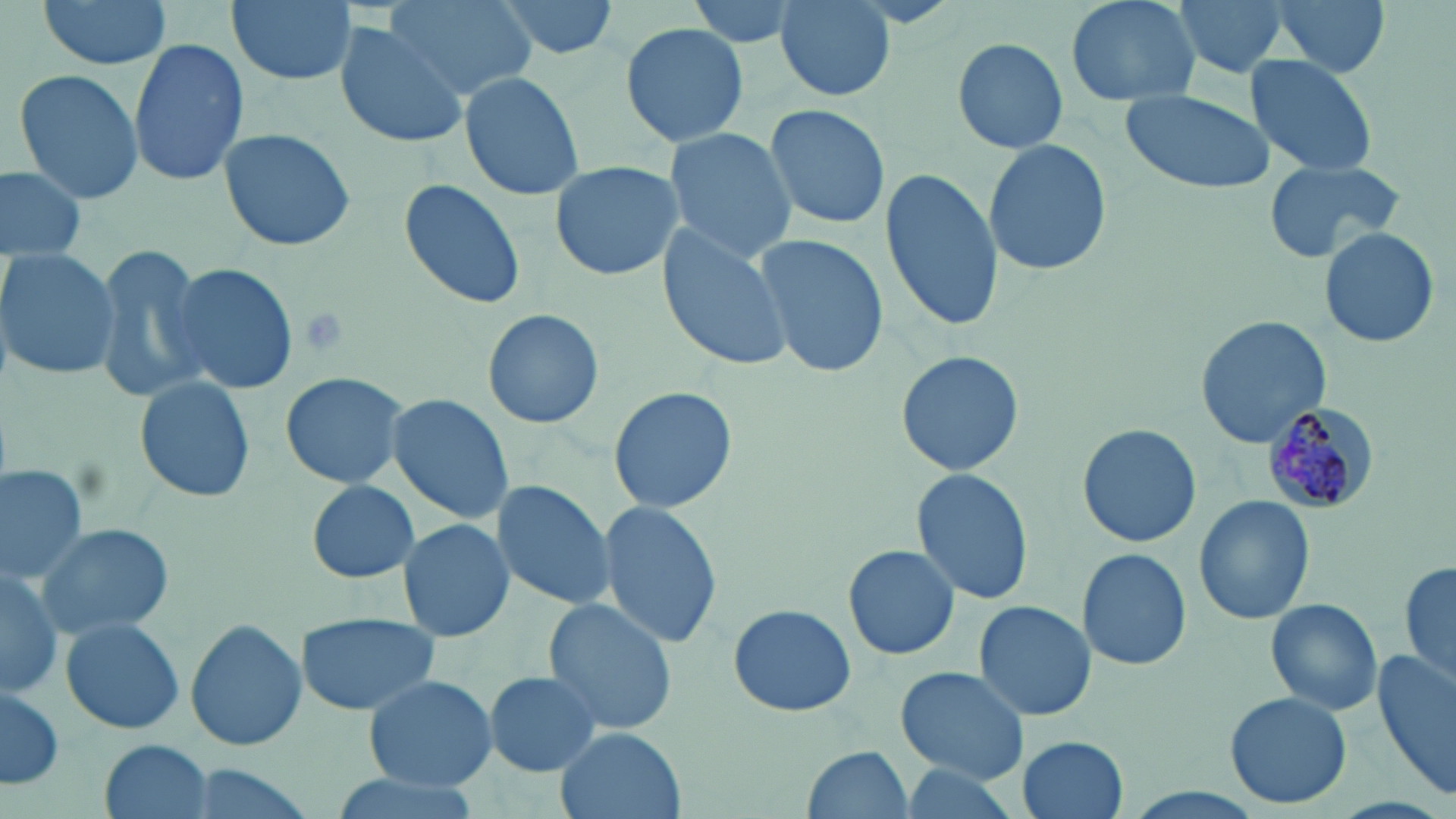
Approximate bounding boxes as (x1, y1, x2, y2) in pixels. Plasmodium malariae-infected red blood cell locations: (1260, 405, 1372, 518). Uninfected red blood cell locations: (35, 0, 172, 74), (224, 0, 358, 89), (490, 0, 623, 59), (685, 0, 808, 50), (773, 0, 896, 101), (1062, 0, 1202, 110), (1172, 0, 1289, 80), (1268, 0, 1390, 79), (389, 1, 532, 100), (622, 22, 749, 147), (333, 23, 469, 148), (950, 35, 1069, 155), (128, 39, 250, 187), (1244, 55, 1378, 175), (13, 69, 146, 206), (463, 71, 586, 200), (1121, 88, 1277, 196), (765, 102, 890, 230), (662, 125, 799, 261), (218, 127, 355, 251), (982, 135, 1112, 277), (1262, 158, 1410, 264), (548, 160, 684, 282), (0, 163, 89, 263), (879, 166, 1002, 334), (399, 178, 527, 310), (657, 221, 796, 374), (1318, 227, 1440, 349), (753, 235, 889, 378), (91, 244, 214, 405), (0, 245, 119, 382), (168, 262, 299, 396), (481, 308, 605, 430), (1195, 316, 1332, 448), (896, 350, 1024, 476), (279, 371, 409, 491), (134, 377, 256, 504), (608, 385, 738, 515), (384, 392, 515, 525), (1078, 424, 1201, 547), (912, 465, 1033, 606), (0, 466, 89, 584), (303, 479, 422, 582), (492, 480, 616, 610), (1195, 496, 1315, 625), (596, 501, 724, 650), (397, 518, 516, 644), (31, 522, 175, 641), (844, 544, 959, 661), (1078, 547, 1191, 672), (1399, 560, 1455, 688), (0, 563, 62, 701), (542, 598, 677, 735), (1265, 598, 1384, 718), (972, 600, 1096, 721), (728, 604, 855, 717), (295, 613, 440, 717), (59, 615, 186, 736), (185, 619, 306, 753), (1372, 652, 1456, 801), (896, 665, 1029, 784), (484, 669, 603, 777), (360, 673, 500, 793), (1, 683, 64, 793), (1225, 691, 1353, 809), (555, 729, 684, 819), (1016, 735, 1130, 818), (99, 738, 213, 818), (803, 744, 916, 817), (174, 764, 320, 817), (898, 764, 1023, 816), (320, 770, 487, 818). Slide-level diagnosis: Plasmodium malariae. Optical microscopy. May-Grünwald-Giemsa-stained preparation. One field of a larger specimen. 1000x magnification. Thin blood film. Image is 1456×819 pixels.